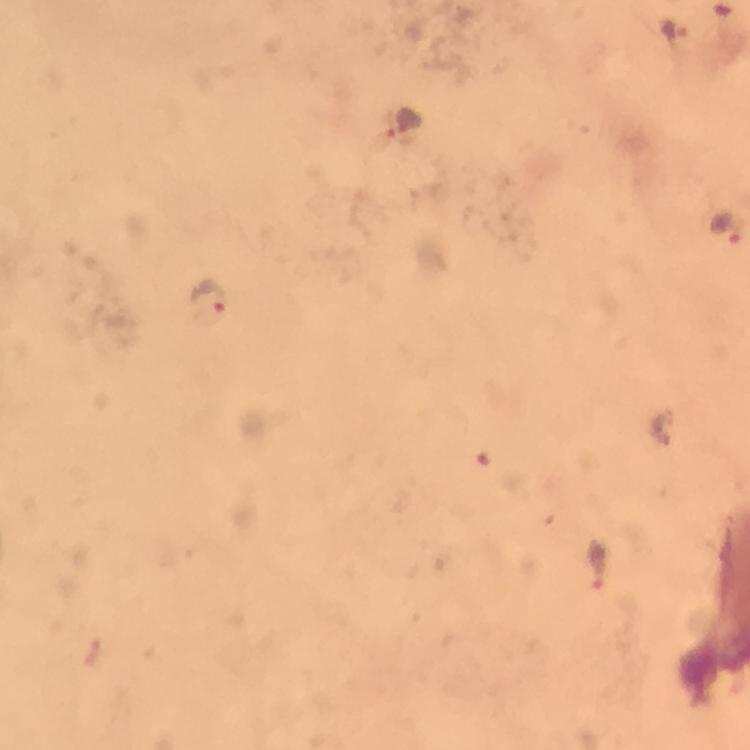
context = from a diagnostic examination for malaria
stain = Giemsa
magnification = 100x
capture = smartphone mounted on the microscope
preparation = thick blood smear
image size = 750×750 pixels
cropped from = a single field of view
immersion oil = used
malaria parasite locations = approximate centers as {x, y} in pixels: {673, 29}, {725, 228}, {211, 297}, {600, 568}, {90, 654}